Assess the morphology of the erythrocytes.
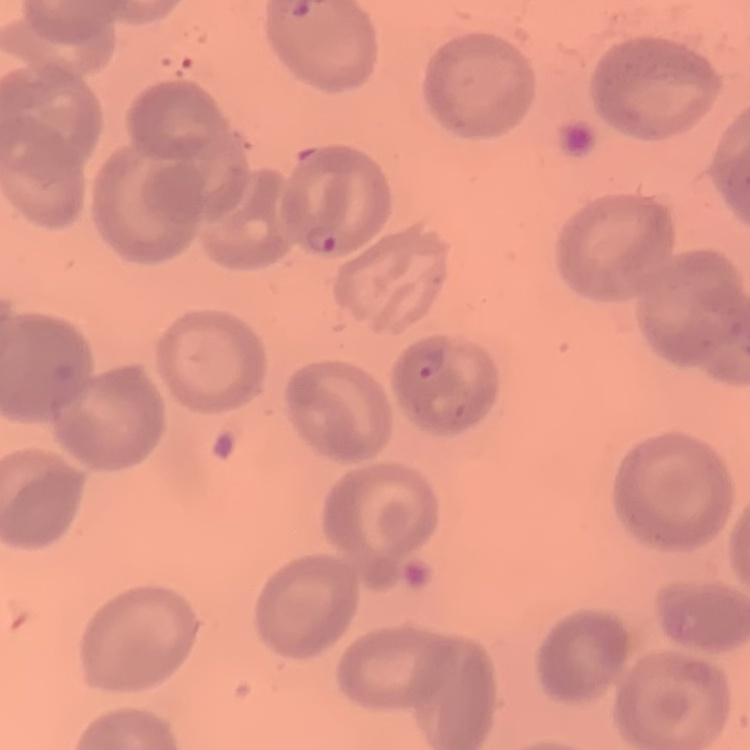
They show no rouleaux formation.

Summary:
  - Preparation: thin peripheral smear
  - Image type: square crop of a larger photomicrograph
  - Stain: Field's or Giemsa